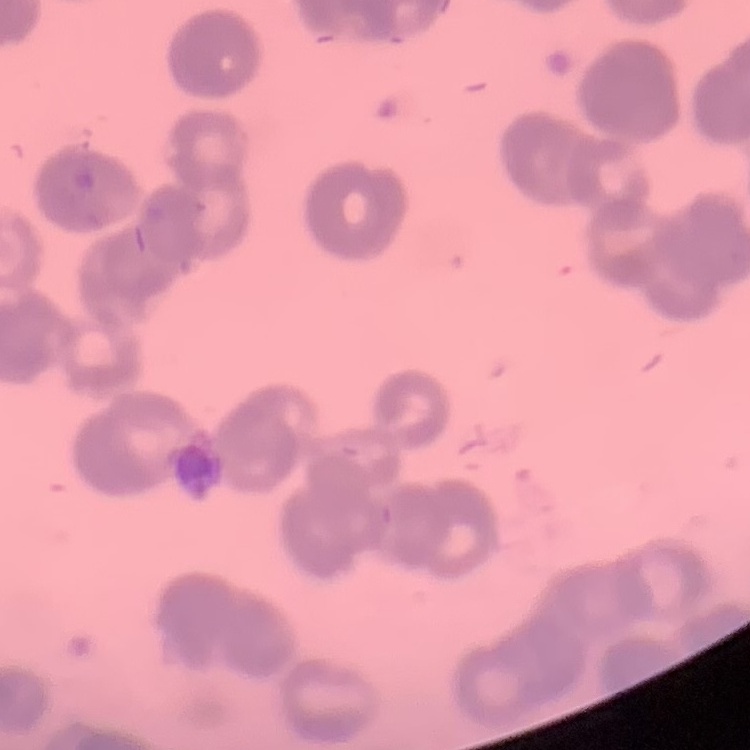
Summary:
  - Erythrocyte morphology: rouleaux formation
  - Image type: square crop of a larger photomicrograph
  - Preparation: thin peripheral smear
  - Stain: Field's or Giemsa